Give the position of every Plasmodium parasite visible.
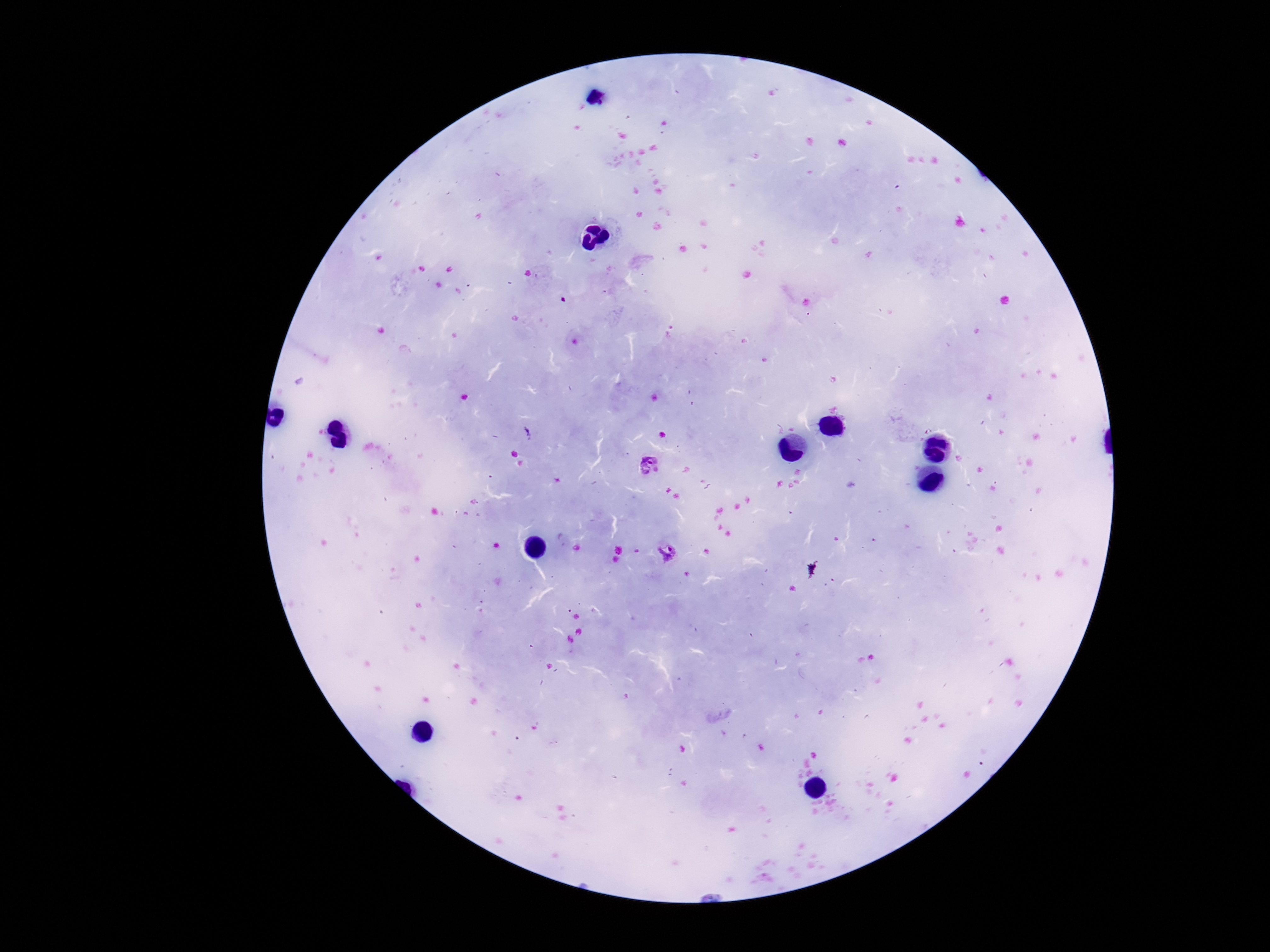

Approximate centers as [x, y] in pixels.
Plasmodium parasites: [648, 466], [667, 553].

{
  "magnification": "100x",
  "capture": "smartphone camera through the microscope eyepiece",
  "stain": "Giemsa",
  "image_size": "1270×952 pixels",
  "patient_malaria_status": "positive",
  "field_of_view": "single",
  "preparation": "thick blood film"
}